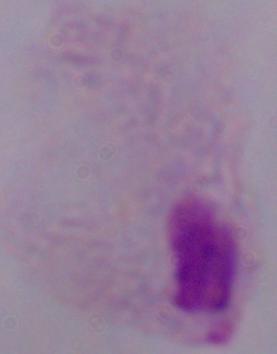

Photomicrograph. 1000x magnification. A trichomonad is seen.